Identify the cell.
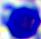
A leukocyte.

modality = photomicrograph
magnification = 400x